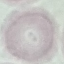
Summary:
  - Malaria status: uninfected
  - Preparation: thin blood smear
  - Image type: automatically extracted cell patch, resized to 64 × 64 pixels
  - Capture: smartphone camera at the microscope eyepiece
  - Stain: Giemsa